Assess this cell for malaria.
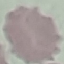
Uninfected.

Thin smear of blood. Acquired by smartphone through the microscope eyepiece. Automatically extracted cell patch, resized to 64 × 64 pixels. Giemsa stain.